Point out each Plasmodium parasite.
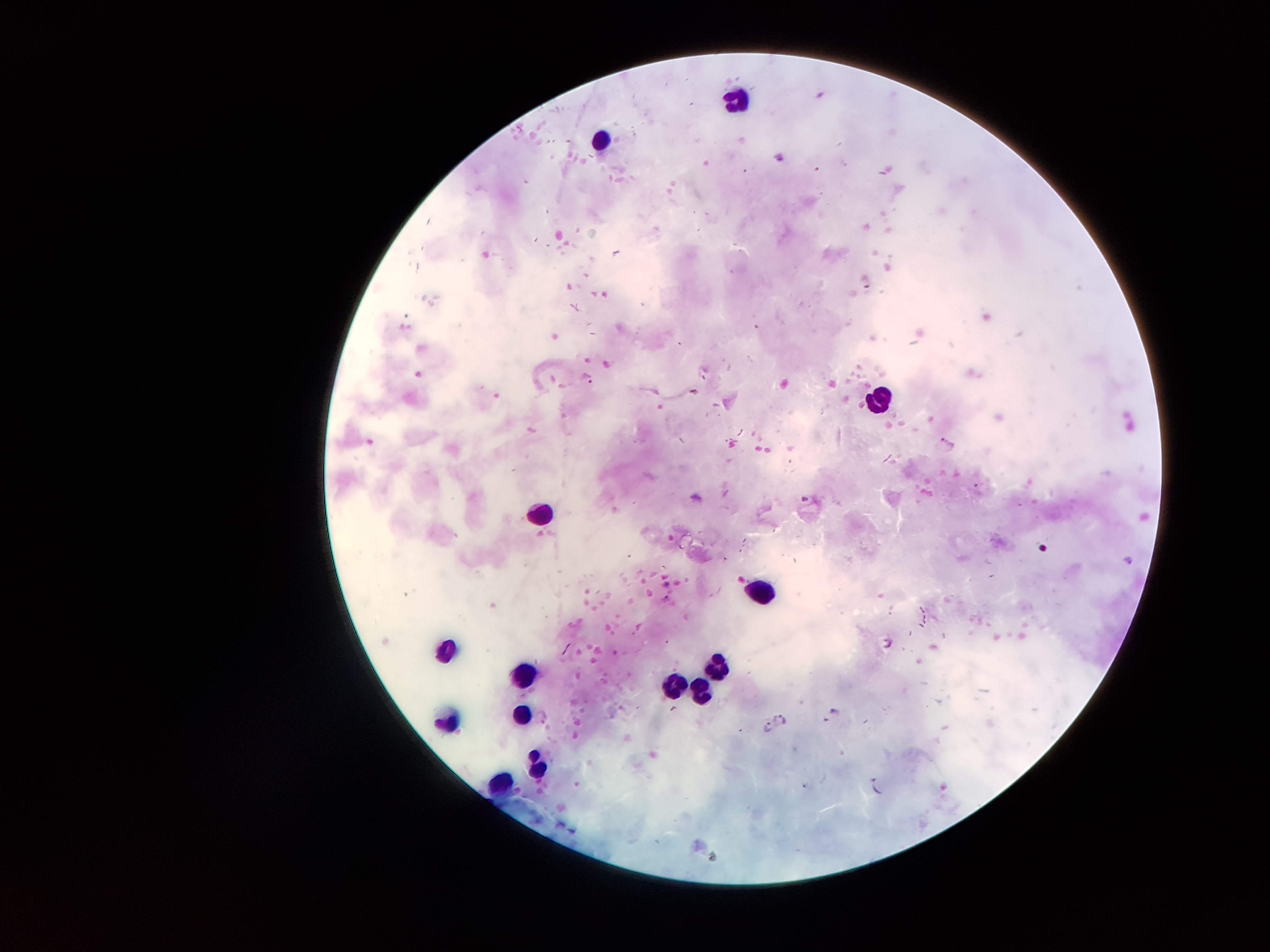

Approximate centers as (x, y) in pixels.
Plasmodium parasites: (589, 379), (947, 444), (889, 643), (834, 711), (779, 719), (766, 728), (877, 784).

Leukocyte locations: (733, 96), (601, 141), (876, 399), (543, 512), (759, 593), (446, 651), (717, 661), (520, 677), (675, 687), (701, 692), (520, 719), (446, 728), (533, 764), (501, 783). Photographed through the microscope eyepiece with a smartphone camera. Thick blood film. 100x magnification. Image is 1270×952 pixels. Patient malaria status: positive for Plasmodium falciparum. Giemsa-stained preparation. One field from this slide.